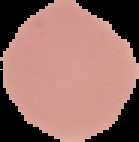
Summary:
  - Image size: 139×142 pixels
  - Preparation: thin blood smear
  - Malaria status: uninfected
  - Image type: segmented cell region on a black background